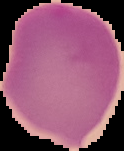
Summary:
  - Image size: 124×151 pixels
  - Preparation: thin blood smear
  - Malaria status: uninfected
  - Image type: segmented cell region on a black background